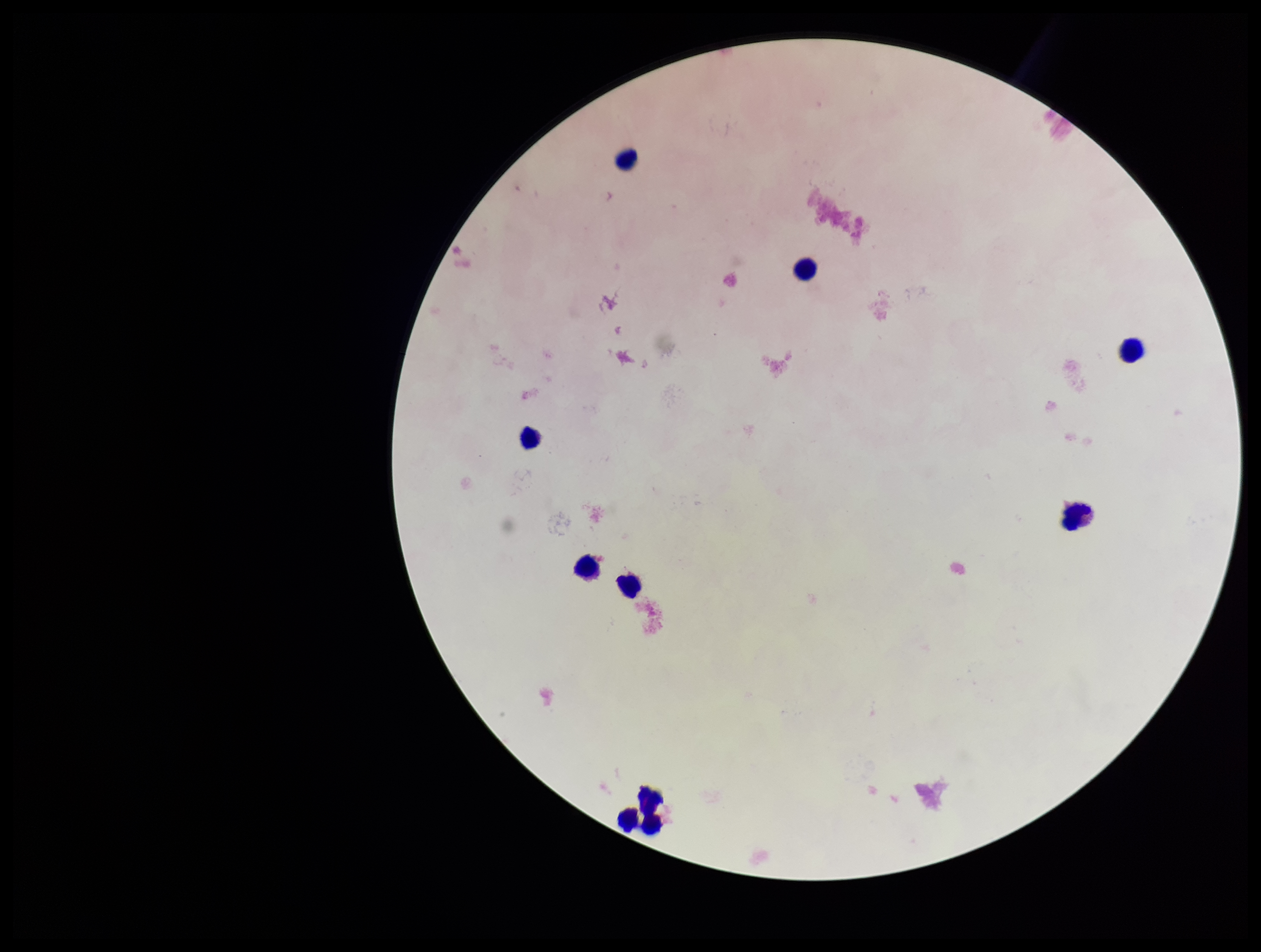
Parasite count: 0. Image is 1261×952 pixels. Preparation: thick. Plasmodium parasites: none seen. Patient malaria status: negative. Stained with Giemsa. Leukocyte count: 9. Smartphone photograph taken through the eyepiece of a microscope. Single field of view.